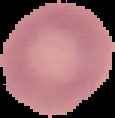

From a thin blood film. Cell region segmented out of the field of view; the surrounding area is masked to black. Image is 115×118 pixels. Result: negative for Plasmodium parasites.